Assess the morphology of the erythrocytes.
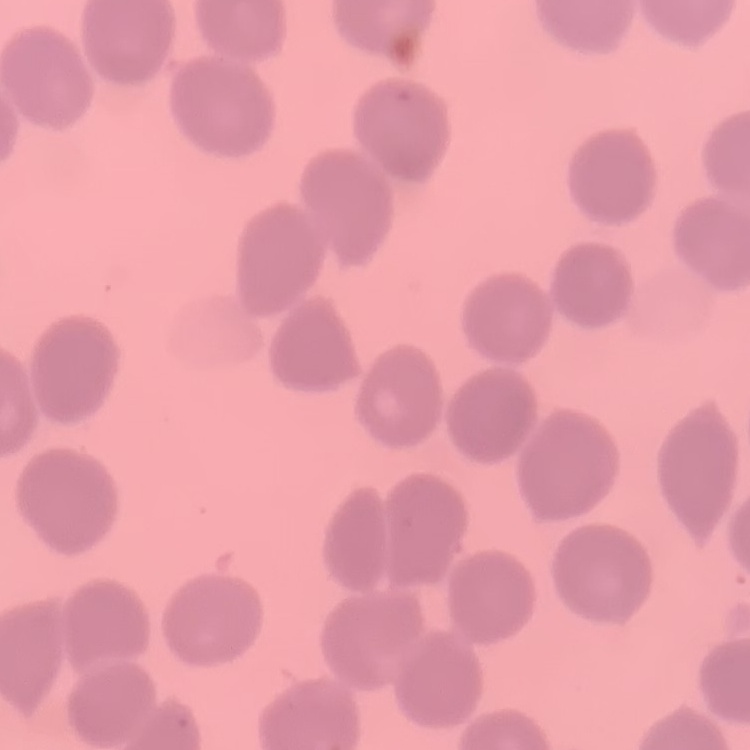
They show no rouleaux formation.

Thin peripheral smear. One tile cut from a larger photomicrograph. Stained with either Field's or Giemsa.